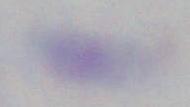

1000x magnification. Toxoplasma gondii is shown. Micrograph.